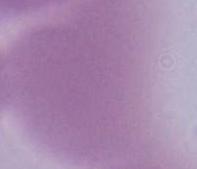
Summary:
  - Identification: erythrocyte
  - Modality: photomicrograph
  - Magnification: 1000x